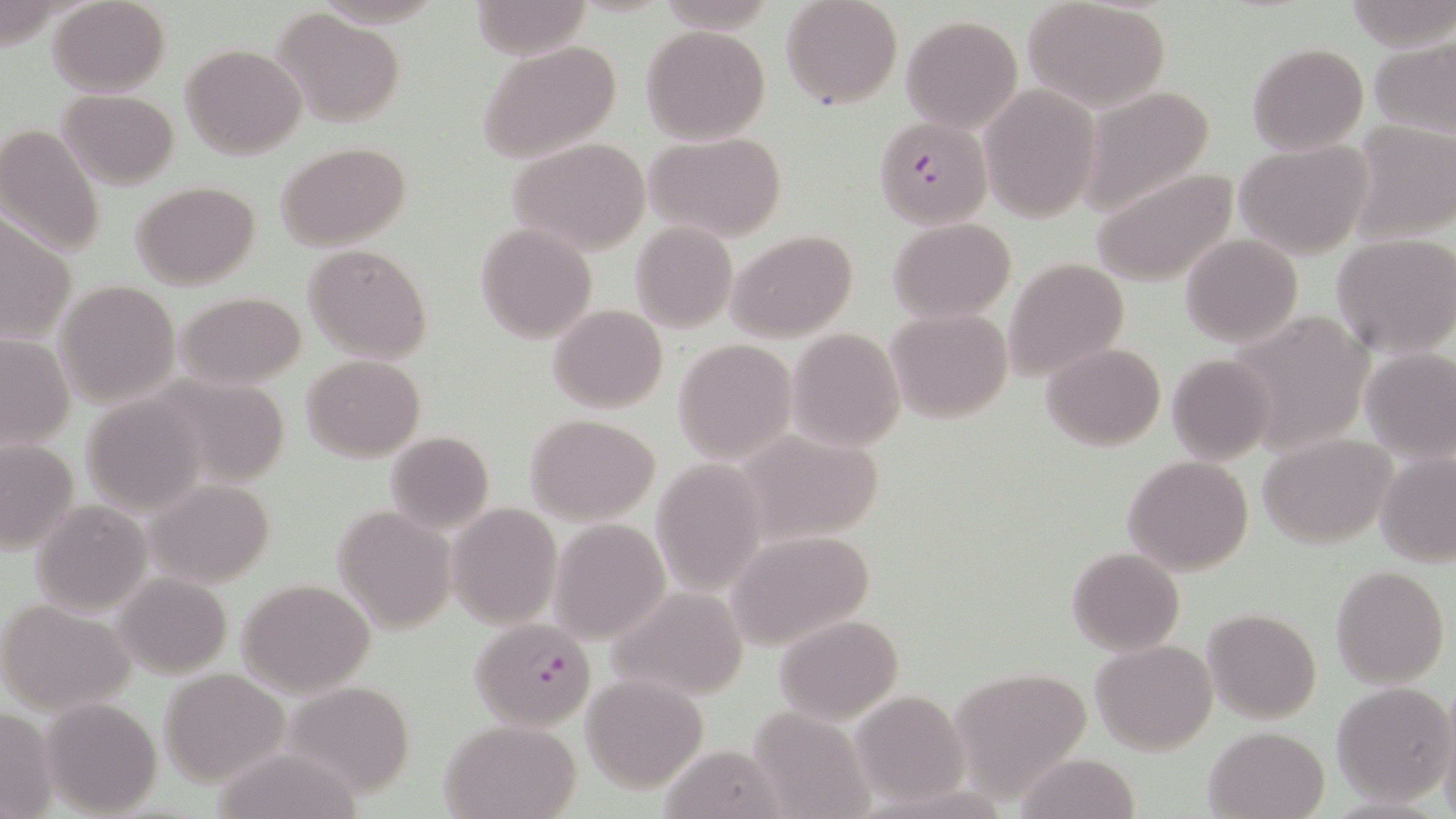

{
  "slide_level_diagnosis": "Plasmodium falciparum",
  "image_size": "1456×819 pixels",
  "modality": "light microscopy",
  "magnification": "1000x",
  "uninfected_red_blood_cell_locations": "approximate bounding boxes as [x1, y1, x2, y2] in pixels: [47, 0, 169, 97], [470, 0, 593, 60], [781, 0, 903, 111], [1023, 1, 1173, 112], [274, 10, 405, 127], [900, 16, 1023, 134], [641, 25, 769, 144], [1369, 37, 1455, 137], [477, 38, 622, 163], [1247, 42, 1369, 155], [180, 43, 307, 161], [978, 84, 1099, 223], [1078, 85, 1218, 218], [57, 90, 180, 188], [1348, 120, 1454, 243], [0, 126, 105, 257], [646, 132, 787, 241], [507, 138, 652, 256], [1235, 140, 1371, 258], [277, 142, 411, 252], [1092, 167, 1238, 288], [132, 181, 260, 289], [0, 217, 78, 346], [888, 217, 1017, 322], [631, 221, 737, 332], [476, 222, 597, 345], [728, 230, 858, 342], [1181, 233, 1304, 347], [1332, 234, 1456, 357], [303, 243, 433, 364], [1004, 258, 1129, 384], [55, 280, 179, 407], [176, 291, 307, 390], [550, 304, 668, 413], [885, 308, 1014, 425], [1228, 311, 1373, 455], [787, 327, 905, 450], [0, 333, 75, 451], [673, 337, 798, 463], [1041, 343, 1165, 450], [1360, 349, 1456, 465], [300, 354, 425, 460], [1165, 354, 1274, 462], [81, 393, 209, 516], [525, 413, 661, 524], [730, 428, 887, 545], [385, 430, 494, 534], [1258, 432, 1396, 549], [0, 438, 78, 554], [1375, 450, 1456, 566], [1123, 455, 1254, 575], [652, 459, 768, 597], [145, 478, 274, 586], [31, 499, 152, 615], [447, 503, 560, 628], [331, 504, 455, 632], [548, 519, 669, 643], [725, 530, 877, 652], [1067, 547, 1184, 656], [1331, 564, 1450, 688], [112, 573, 232, 679], [238, 579, 376, 697], [607, 586, 750, 702], [0, 601, 137, 713], [1203, 608, 1322, 724], [775, 614, 903, 724], [1091, 618, 1325, 734], [1092, 639, 1217, 754], [159, 667, 291, 785], [950, 667, 1093, 790], [580, 674, 707, 793], [284, 681, 417, 798], [1331, 682, 1453, 806], [850, 690, 971, 807], [42, 697, 163, 817], [0, 705, 58, 817], [748, 706, 875, 817], [1438, 715, 1456, 819], [437, 718, 582, 819], [1203, 725, 1330, 818], [659, 745, 786, 817], [1014, 754, 1142, 818]",
  "preparation": "thin blood film",
  "plasmodium_falciparum_infected_red_blood_cell_locations": "approximate bounding boxes as [x1, y1, x2, y2] in pixels: [875, 118, 992, 230], [470, 618, 597, 732]",
  "field_of_view": "single",
  "stain": "May-Grünwald-Giemsa"
}